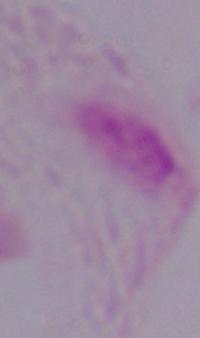

Photomicrograph. A trichomonad is shown. Captured at 1000x magnification.